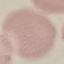
Result: no malaria parasites detected. Thin blood film. Acquired by smartphone through the microscope eyepiece. Automatically extracted cell patch, resized to 64 × 64 pixels. Giemsa-stained preparation.